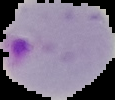

preparation = thin blood film
image type = segmented cell region on a black background
result = malaria parasites identified
image size = 115×100 pixels